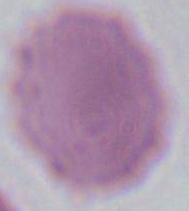

modality: photomicrograph
identification: erythrocyte
magnification: 1000x